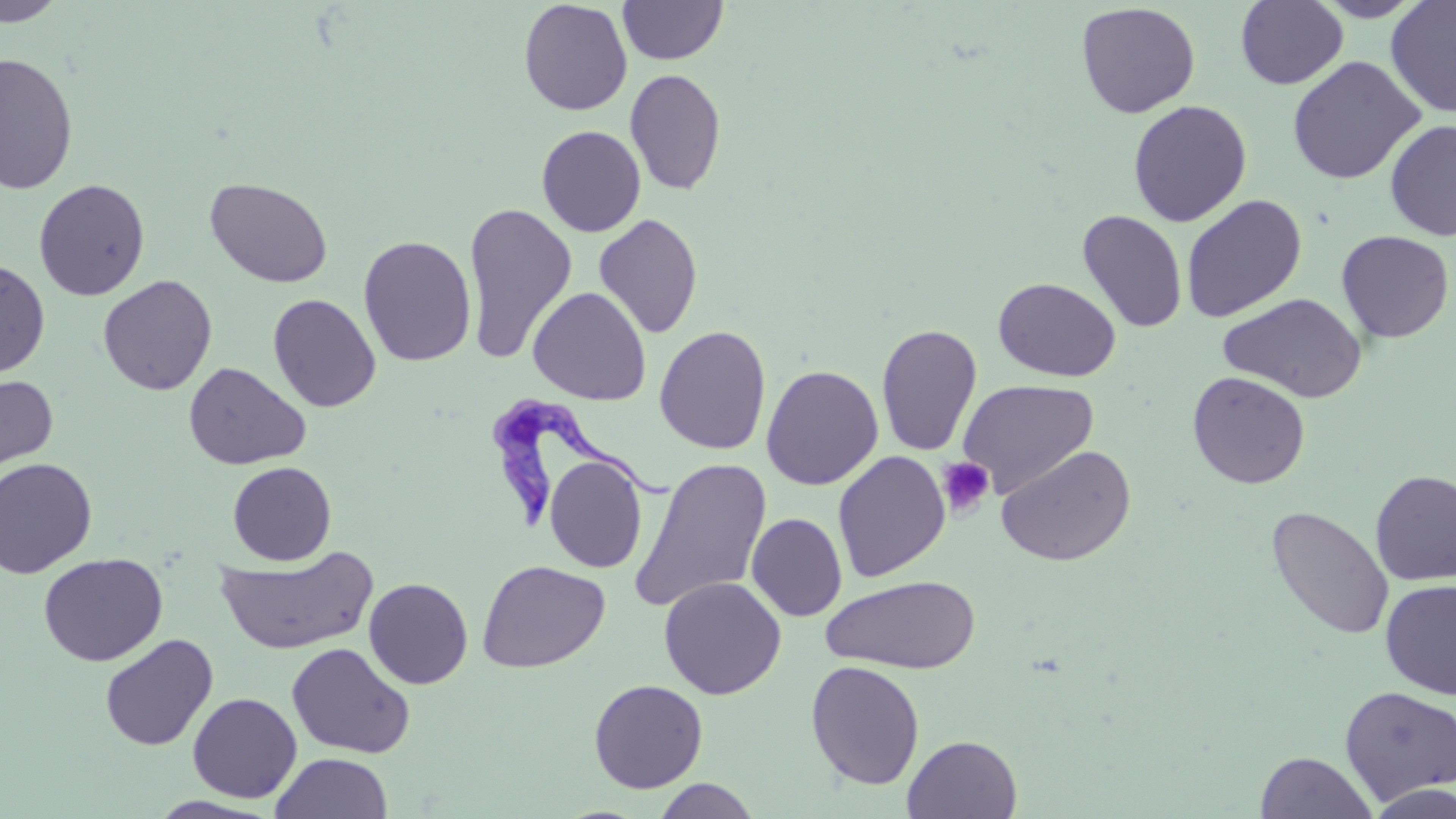

{
  "slide_level_diagnosis": "Trypanosoma brucei",
  "stain": "May-Grünwald-Giemsa",
  "field_of_view": "single",
  "modality": "optical microscopy",
  "trypanosoma_brucei_locations": "approximate bounding boxes as (x1, y1, x2, y2) in pixels: (486, 393, 670, 529)",
  "platelet_locations": "approximate bounding boxes as (x1, y1, x2, y2) in pixels: (936, 456, 995, 517)",
  "image_size": "1456×819 pixels",
  "uninfected_red_blood_cell_locations": "approximate bounding boxes as (x1, y1, x2, y2) in pixels: (0, 0, 69, 27), (518, 0, 632, 116), (618, 0, 728, 65), (1236, 0, 1349, 90), (1311, 0, 1428, 22), (1385, 1, 1456, 118), (1075, 3, 1201, 119), (0, 52, 79, 194), (1287, 55, 1426, 185), (625, 68, 727, 196), (1127, 99, 1252, 227), (1384, 119, 1456, 241), (536, 125, 647, 238), (204, 176, 334, 288), (33, 178, 151, 301), (1180, 194, 1307, 323), (463, 202, 577, 366), (1077, 210, 1188, 333), (594, 214, 704, 340), (1336, 230, 1454, 343), (358, 234, 477, 367), (0, 258, 51, 378), (97, 274, 218, 396), (993, 277, 1120, 382), (528, 286, 652, 406), (1219, 292, 1368, 403), (267, 293, 381, 413), (876, 323, 982, 457), (654, 325, 771, 455), (183, 361, 311, 470), (761, 364, 883, 490), (0, 371, 59, 486), (1187, 371, 1310, 489), (958, 379, 1099, 498), (996, 444, 1137, 567), (832, 451, 951, 582), (544, 455, 648, 573), (0, 457, 98, 578), (630, 457, 773, 614), (227, 461, 337, 565), (1370, 469, 1456, 586), (1265, 506, 1395, 640), (746, 513, 847, 621), (215, 546, 378, 655), (38, 552, 168, 667), (476, 559, 610, 673), (822, 575, 980, 674), (363, 577, 473, 689), (659, 577, 786, 699), (1379, 579, 1456, 699), (100, 633, 218, 750), (286, 642, 415, 759), (806, 660, 925, 790), (588, 678, 708, 793), (1339, 685, 1456, 805), (187, 692, 302, 803), (902, 734, 1023, 818), (1255, 751, 1378, 819), (271, 752, 393, 819), (652, 778, 761, 819), (1364, 780, 1456, 818), (147, 795, 280, 818)",
  "magnification": "1000x",
  "preparation": "thin blood smear"
}